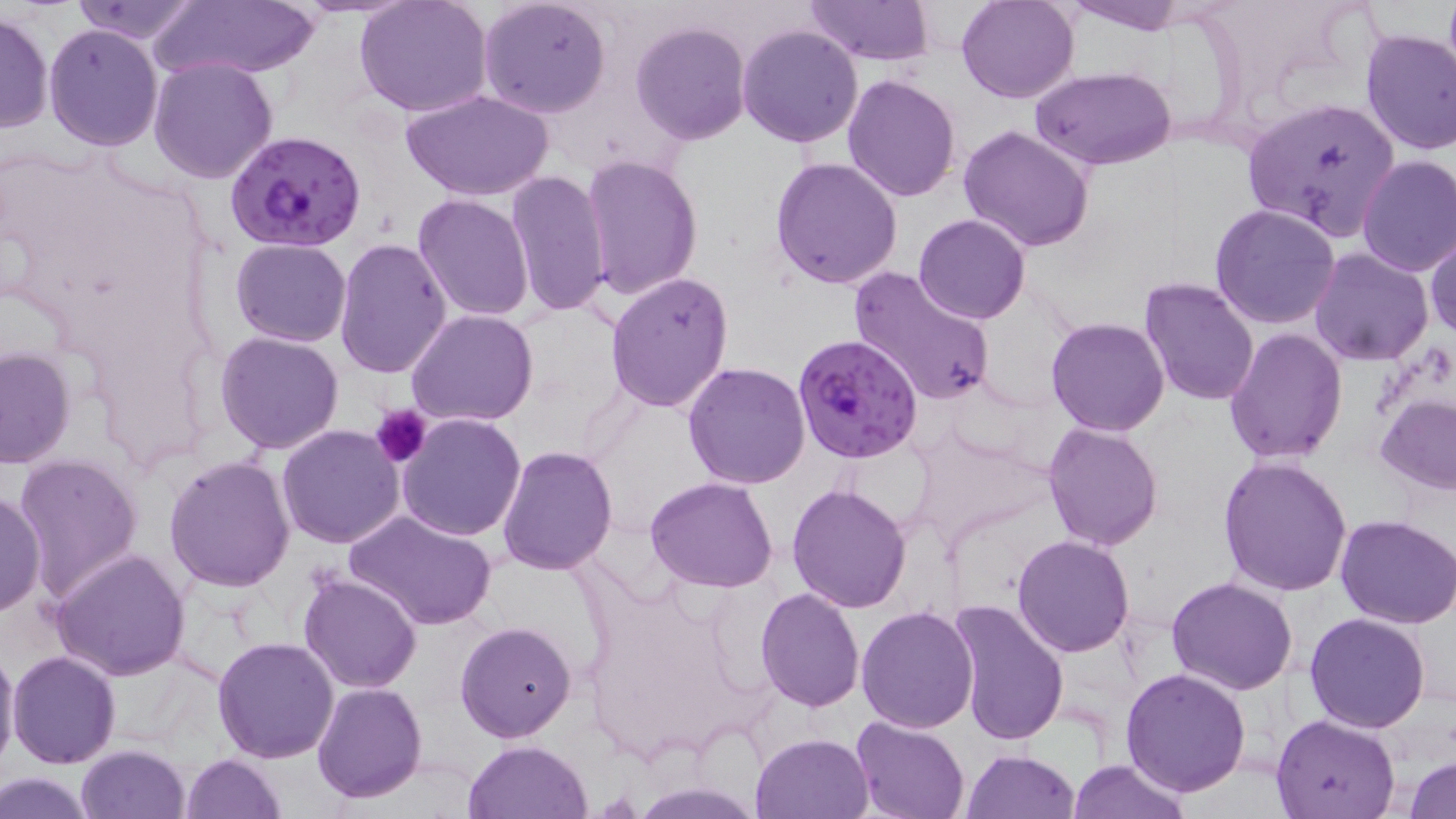

{
  "plasmodium_falciparum_infected_red_blood_cell_locations": "approximate bounding boxes as [x1, y1, x2, y2] in pixels: [226, 128, 369, 252], [791, 334, 923, 462]",
  "slide_level_diagnosis": "Plasmodium falciparum",
  "magnification": "1000x",
  "stain": "May-Grünwald-Giemsa",
  "platelet_locations": "approximate bounding boxes as [x1, y1, x2, y2] in pixels: [371, 404, 430, 466]",
  "modality": "light microscopy",
  "preparation": "thin blood film",
  "uninfected_red_blood_cell_locations": "approximate bounding boxes as [x1, y1, x2, y2] in pixels: [354, 0, 493, 119], [479, 0, 612, 119], [802, 0, 936, 67], [956, 0, 1078, 103], [1064, 0, 1188, 35], [68, 1, 202, 44], [155, 1, 319, 81], [0, 11, 54, 135], [631, 19, 752, 146], [44, 24, 163, 152], [737, 24, 863, 148], [1359, 28, 1456, 156], [148, 57, 278, 184], [1030, 66, 1177, 168], [843, 75, 961, 202], [403, 90, 552, 202], [1243, 96, 1401, 239], [957, 123, 1097, 251], [581, 154, 703, 302], [1356, 154, 1456, 276], [770, 156, 904, 289], [505, 171, 612, 316], [412, 193, 533, 322], [1209, 203, 1342, 331], [913, 214, 1031, 325], [1426, 232, 1456, 344], [334, 238, 452, 378], [230, 239, 352, 348], [1310, 247, 1434, 366], [848, 266, 995, 407], [604, 271, 735, 413], [1137, 277, 1260, 406], [406, 309, 538, 428], [1045, 316, 1172, 437], [1224, 329, 1348, 465], [214, 331, 344, 454], [0, 346, 76, 469], [682, 360, 812, 488], [1375, 395, 1456, 494], [397, 412, 526, 541], [1043, 422, 1165, 551], [277, 425, 406, 549], [909, 428, 1052, 549], [496, 446, 618, 574], [12, 453, 144, 599], [1217, 455, 1353, 597], [164, 456, 297, 593], [646, 476, 778, 592], [786, 482, 912, 613], [1, 487, 47, 618], [344, 510, 497, 632], [1336, 513, 1456, 627], [1012, 534, 1137, 657], [50, 548, 191, 681], [298, 572, 420, 692], [1166, 576, 1297, 695], [754, 589, 864, 711], [947, 599, 1070, 745], [857, 607, 980, 734], [1305, 611, 1433, 732], [454, 619, 577, 741], [211, 637, 340, 762], [0, 642, 21, 777], [9, 650, 121, 769], [1120, 667, 1252, 795], [313, 683, 426, 804], [1270, 713, 1401, 819], [849, 716, 970, 819], [751, 732, 875, 819], [465, 740, 592, 819], [75, 744, 190, 819], [961, 750, 1081, 818], [178, 753, 287, 819], [1406, 757, 1456, 818], [1067, 759, 1191, 819], [1, 772, 96, 817], [633, 782, 759, 818]",
  "field_of_view": "single",
  "image_size": "1456×819 pixels"
}